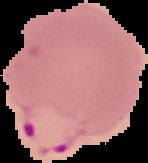 The area outside the segmented cell region is set to black. Image is 148×163 pixels. From a thin blood smear. Result: Plasmodium parasites identified.